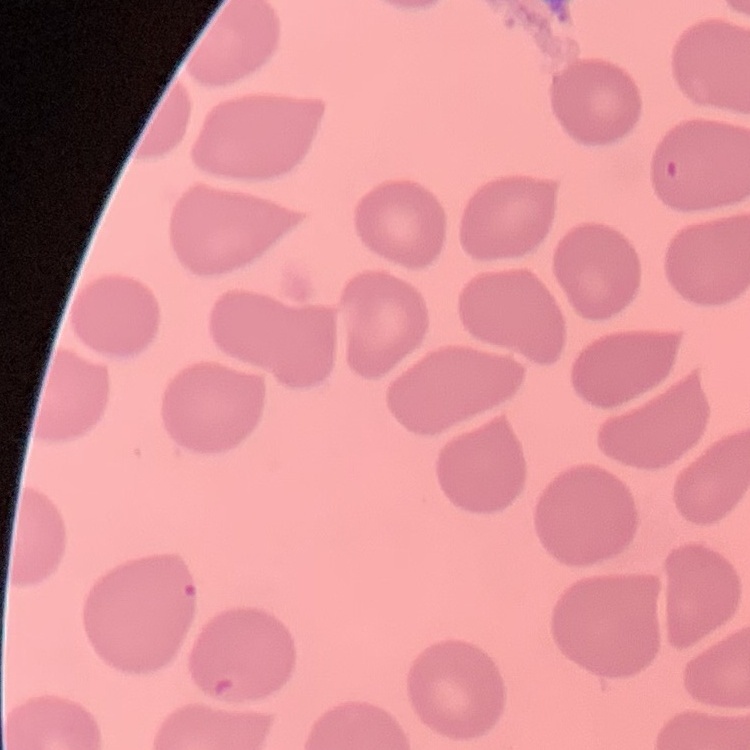

The red blood cells show no rouleaux formation. Thin blood smear. Square crop of a larger photomicrograph. Field's or Giemsa stain.